Classify this cell by malaria status.
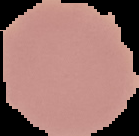

It is uninfected.

Summary:
  - Image size: 139×136 pixels
  - Image type: segmented cell region with the area outside set to black
  - Preparation: thin blood film